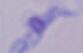

identification = trypanosome
magnification = 1000x
modality = micrograph